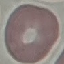
Malaria status: uninfected. Thin smear of blood. Cell patch, automatically extracted from a larger field of view and resized to 64 × 64 pixels. Photographed with a smartphone camera at the microscope eyepiece. Giemsa stain.